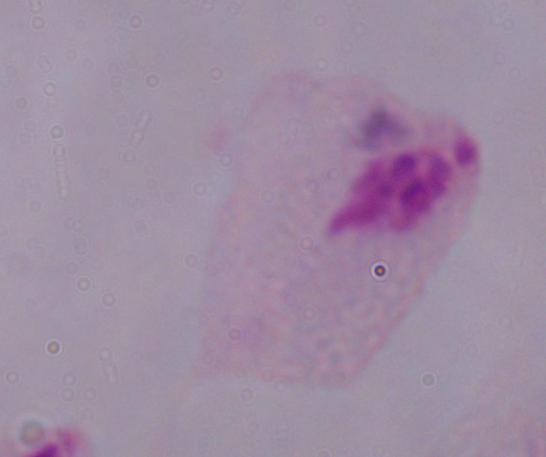

modality = photomicrograph
magnification = 1000x
identification = trichomonad